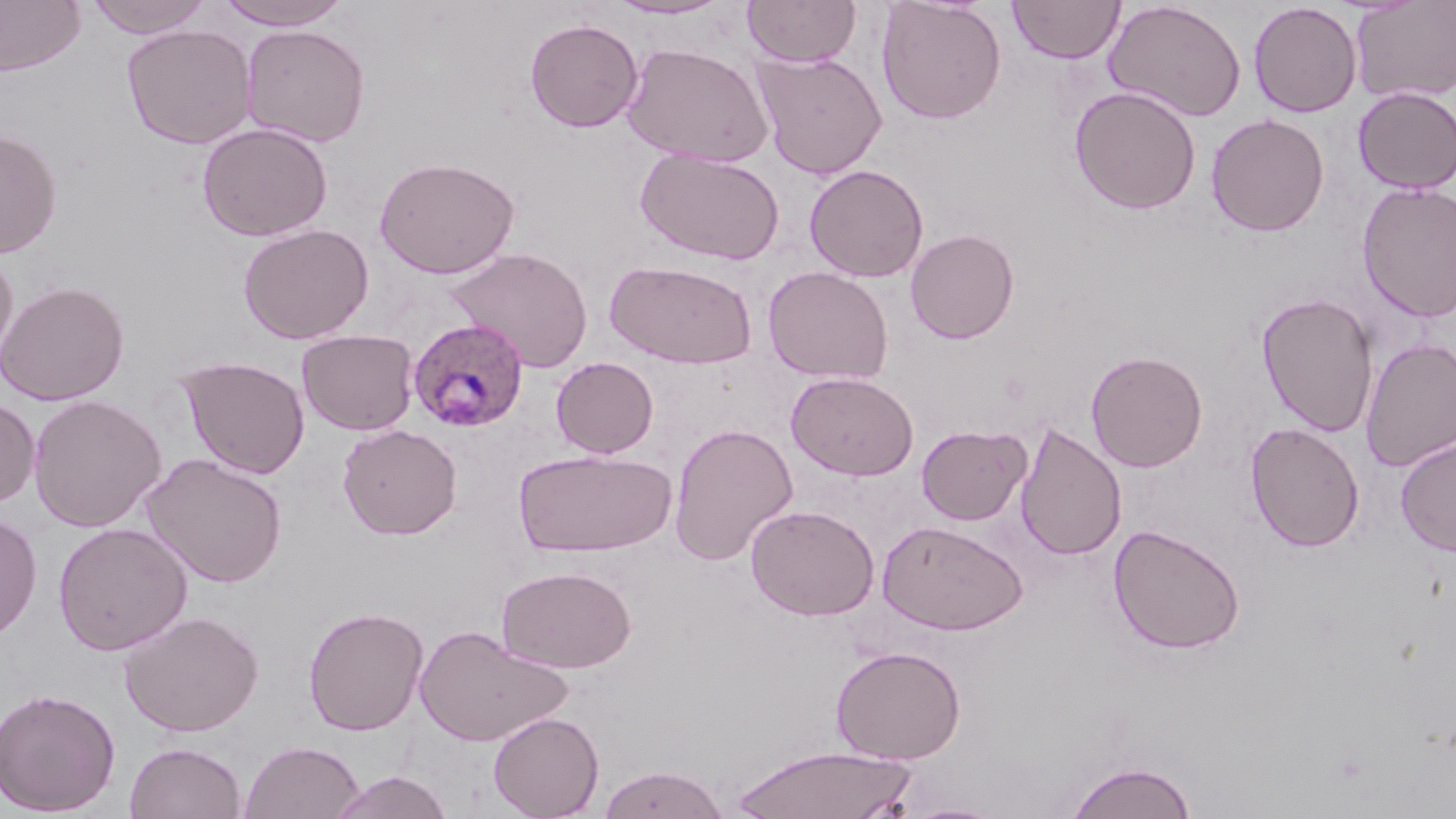
slide-level diagnosis = Plasmodium ovale
image size = 1456×819 pixels
Plasmodium ovale-infected red blood cell locations = approximate bounding boxes as (x1, y1, x2, y2) in pixels: (411, 319, 533, 434)
field of view = one of a larger specimen
modality = optical microscopy
stain = May-Grünwald-Giemsa
magnification = 1000x
preparation = thin blood film
uninfected red blood cell locations = approximate bounding boxes as (x1, y1, x2, y2) in pixels: (0, 0, 85, 76), (84, 0, 213, 39), (216, 0, 352, 29), (605, 0, 735, 20), (742, 0, 862, 67), (1008, 0, 1125, 64), (1350, 0, 1456, 103), (876, 1, 1007, 125), (1103, 1, 1247, 122), (1248, 2, 1362, 118), (525, 18, 644, 132), (122, 23, 257, 149), (240, 24, 370, 147), (621, 42, 773, 167), (753, 51, 888, 178), (1069, 86, 1201, 215), (1353, 86, 1456, 194), (1206, 113, 1330, 236), (197, 122, 333, 241), (0, 128, 62, 259), (634, 148, 785, 265), (374, 156, 520, 278), (804, 164, 929, 282), (1357, 182, 1456, 323), (238, 223, 374, 344), (905, 228, 1019, 344), (446, 247, 594, 372), (0, 249, 18, 369), (606, 259, 758, 369), (763, 265, 894, 385), (0, 280, 130, 406), (1255, 293, 1379, 437), (296, 329, 419, 436), (1360, 338, 1456, 473), (1085, 350, 1208, 471), (177, 355, 311, 479), (551, 356, 659, 458), (786, 371, 919, 481), (28, 394, 166, 532), (0, 397, 40, 509), (1245, 422, 1365, 552), (668, 423, 798, 566), (1015, 423, 1126, 561), (337, 424, 462, 539), (916, 425, 1031, 525), (1395, 437, 1456, 557), (512, 447, 675, 557), (142, 452, 288, 588), (746, 504, 879, 621), (0, 513, 42, 642), (876, 519, 1029, 635), (53, 522, 193, 655), (1109, 524, 1246, 655), (496, 565, 637, 673), (302, 605, 429, 736), (118, 610, 264, 737), (414, 625, 570, 747), (830, 645, 967, 764), (0, 686, 121, 816), (487, 711, 604, 819), (239, 740, 365, 819), (124, 741, 247, 819), (729, 744, 920, 819), (1065, 760, 1198, 819), (596, 765, 731, 819), (328, 770, 455, 819), (900, 800, 1009, 819)